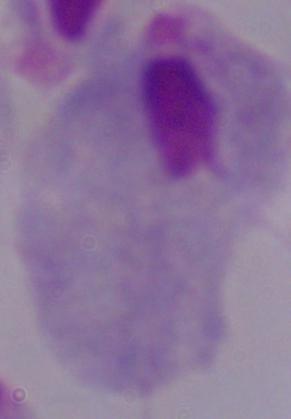 A trichomonad is shown. Micrograph. 1000x magnification.